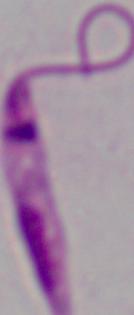 Micrograph. Captured at 1000x magnification. A Leishmania parasite is shown.